Identify the cell.
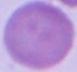

This is an erythrocyte.

1000x magnification. Photomicrograph.